Assess this cell for malaria.
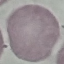
Uninfected.

Summary:
  - Preparation: thin smear
  - Image type: cell patch, automatically extracted from a larger field of view and resized to 64 × 64 pixels
  - Capture: smartphone through the microscope eyepiece
  - Stain: Giemsa